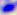
modality = micrograph
identification = Toxoplasma gondii
magnification = 400x